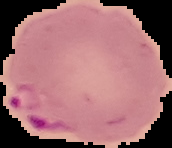
image size = 172×148 pixels
preparation = thin blood film
result = malaria parasites detected
image type = cell region segmented out of the field of view; surrounding area masked to black